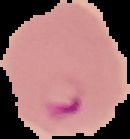 Image is 130×139 pixels. From a thin blood smear. Result: malaria parasites detected. Cell region segmented out of the field of view; the surrounding area is masked to black.